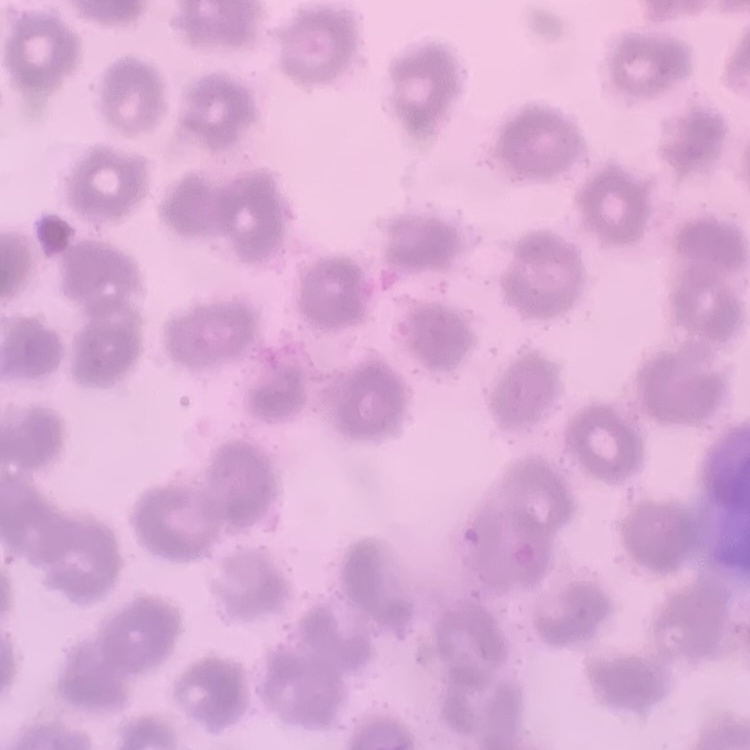

red_blood_cell_morphology: no rouleaux formation
stain: Field's or Giemsa
preparation: thin peripheral smear
image_type: square crop of a larger photomicrograph